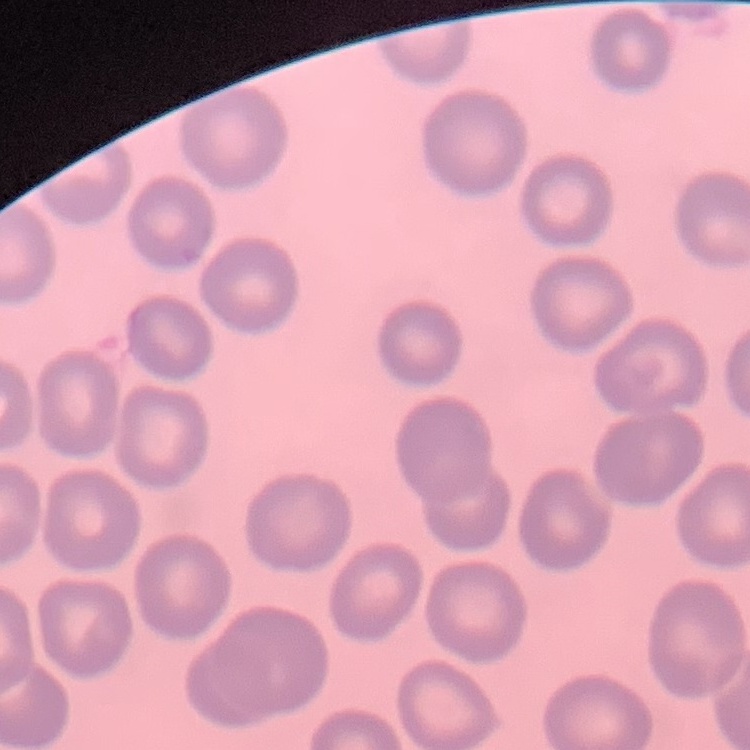
erythrocyte morphology = no rouleaux formation
preparation = thin peripheral smear
stain = Field's or Giemsa
image type = one tile cut from a larger photomicrograph